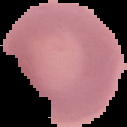
Summary:
  - Malaria status: uninfected
  - Image size: 127×127 pixels
  - Image type: cell region segmented out of the field of view; surrounding area masked to black
  - Preparation: thin blood smear